Point out each Plasmodium parasite.
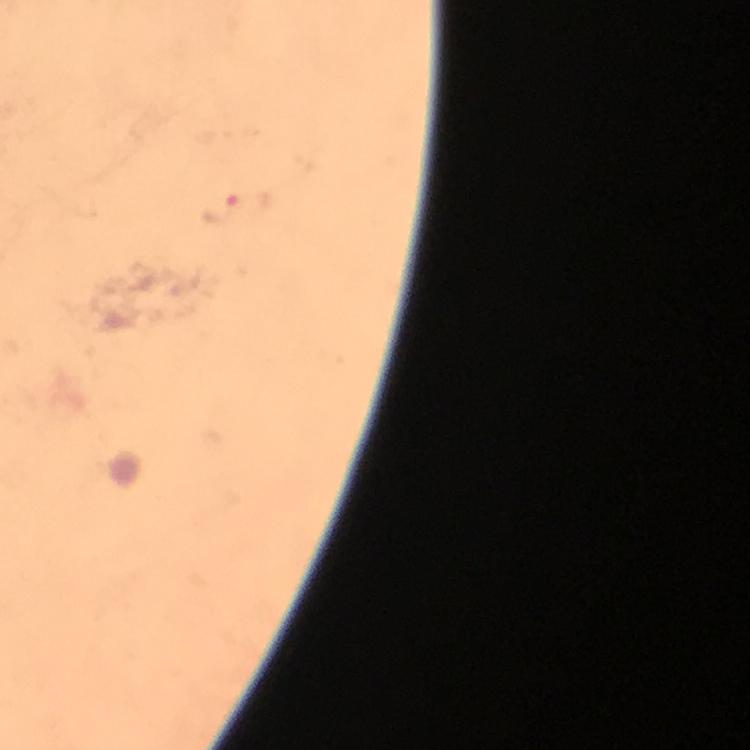
Approximate centers as {x, y} in pixels.
Plasmodium parasites: {241, 206}.

image_size: 750×750 pixels
preparation: thick blood film
cropped_from: a single field of view
immersion_oil: applied
context: from a diagnostic examination for malaria
stain: Giemsa
capture: smartphone camera through the microscope
magnification: 100x